Assess this cell for malaria.
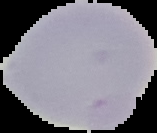
It is uninfected.

image type = cell region segmented out of the field of view; surrounding area masked to black
preparation = thin blood film
image size = 157×133 pixels